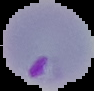

Summary:
  - Image type: segmented cell region on a black background
  - Preparation: thin blood film
  - Result: malaria parasites identified
  - Image size: 94×91 pixels